State which parasite is depicted.
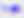

Toxoplasma gondii.

Summary:
  - Modality: photomicrograph
  - Magnification: 400x